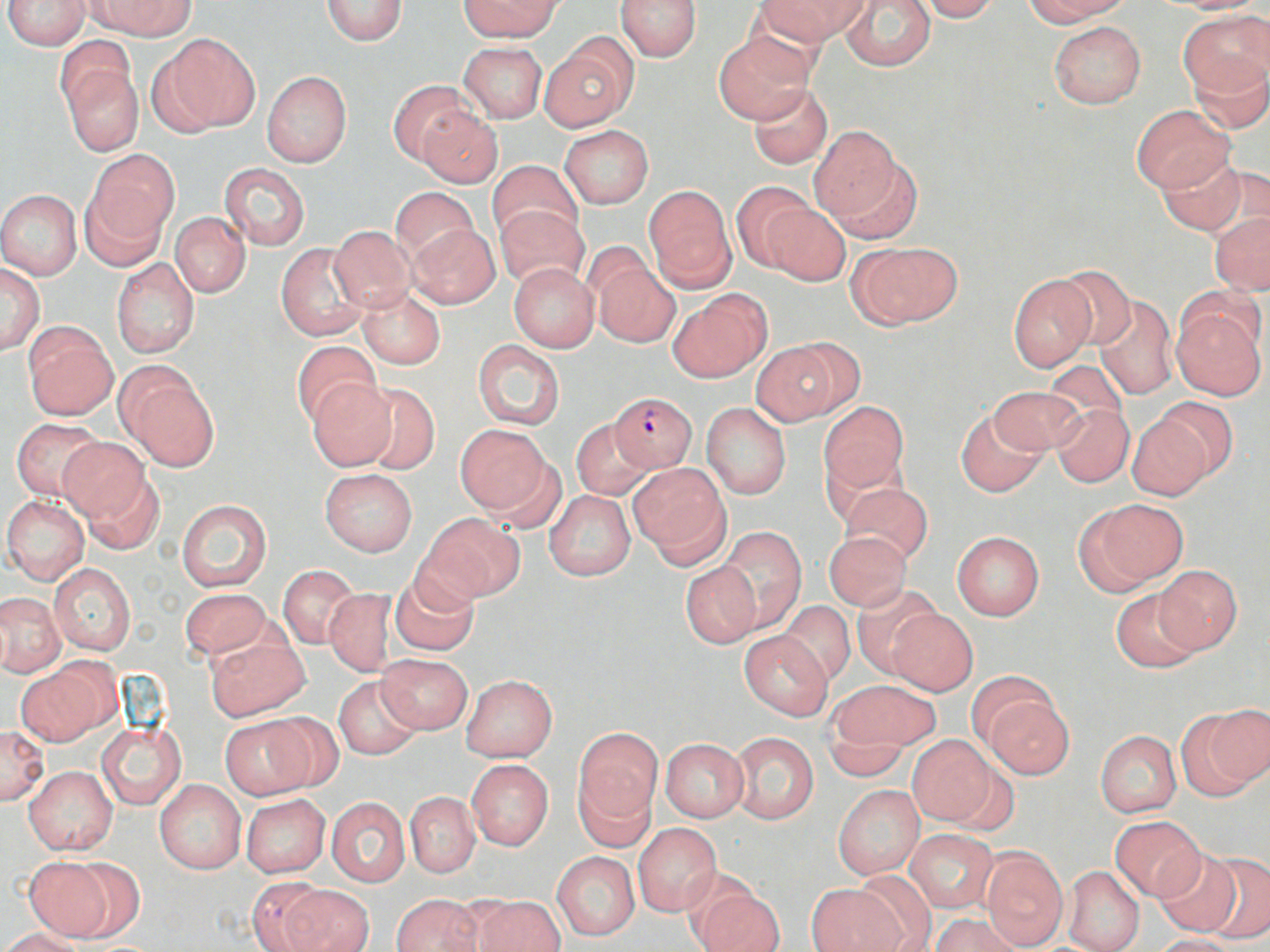

Approximate bounding boxes as [x1, y1, x2, y2] in pixels. Uninfected red blood cell locations: [4, 0, 90, 51], [91, 0, 193, 37], [321, 0, 408, 45], [461, 0, 561, 40], [615, 0, 703, 61], [758, 0, 868, 45], [915, 0, 999, 21], [1022, 0, 1129, 26], [1164, 0, 1267, 14], [839, 1, 935, 71], [1180, 10, 1268, 93], [1048, 21, 1146, 108], [160, 34, 258, 131], [714, 34, 812, 123], [541, 36, 638, 132], [459, 42, 547, 123], [58, 50, 143, 157], [1186, 56, 1270, 134], [261, 71, 352, 167], [388, 80, 469, 165], [748, 83, 833, 169], [1132, 104, 1232, 193], [417, 107, 503, 188], [808, 124, 901, 221], [560, 125, 653, 208], [85, 152, 177, 251], [829, 153, 922, 245], [1156, 153, 1250, 235], [487, 160, 582, 244], [218, 163, 310, 251], [731, 181, 813, 270], [643, 185, 735, 291], [390, 187, 480, 264], [0, 190, 82, 280], [764, 203, 851, 286], [497, 205, 588, 290], [1210, 211, 1270, 295], [171, 212, 250, 297], [408, 223, 499, 308], [328, 226, 416, 311], [851, 241, 960, 329], [275, 242, 373, 342], [111, 257, 201, 360], [592, 259, 680, 348], [508, 263, 599, 352], [0, 264, 44, 354], [1049, 264, 1140, 351], [1007, 272, 1096, 371], [355, 286, 446, 369], [669, 291, 771, 382], [1093, 295, 1178, 399], [1172, 299, 1267, 399], [23, 326, 117, 420], [291, 339, 381, 428], [751, 340, 847, 425], [472, 341, 565, 430], [116, 365, 217, 470], [307, 380, 397, 469], [354, 382, 441, 475], [986, 385, 1086, 456], [1151, 397, 1237, 485], [820, 401, 908, 493], [1051, 402, 1133, 486], [701, 404, 791, 500], [955, 408, 1048, 497], [1127, 413, 1214, 501], [11, 418, 103, 500], [571, 419, 656, 501], [454, 424, 553, 516], [58, 436, 147, 523], [631, 465, 730, 565], [79, 466, 166, 555], [320, 469, 417, 555], [839, 483, 933, 565], [545, 490, 636, 581], [2, 495, 89, 584], [175, 497, 272, 593], [1078, 497, 1189, 592], [421, 513, 523, 604], [716, 526, 806, 632], [823, 530, 911, 610], [952, 531, 1045, 620], [49, 562, 136, 655], [680, 562, 760, 648], [1154, 564, 1242, 653], [278, 565, 360, 648], [389, 570, 480, 657], [851, 582, 942, 676], [1111, 586, 1205, 673], [178, 587, 272, 662], [323, 589, 395, 676], [0, 593, 66, 675], [779, 601, 855, 685], [885, 607, 978, 695], [739, 630, 833, 720], [203, 633, 310, 722], [375, 654, 472, 734], [17, 659, 113, 744], [460, 675, 557, 762], [333, 677, 424, 760], [825, 679, 941, 757], [979, 688, 1075, 779], [1183, 704, 1270, 797], [219, 715, 318, 800], [97, 721, 185, 809], [0, 724, 48, 804], [574, 728, 661, 828], [1096, 730, 1181, 817], [731, 733, 818, 824], [907, 737, 998, 827], [660, 738, 747, 822], [466, 759, 554, 851], [24, 766, 117, 854], [575, 770, 656, 853], [156, 780, 245, 874], [833, 786, 924, 879], [405, 792, 480, 877], [242, 793, 330, 878], [326, 797, 410, 887], [1108, 815, 1205, 901], [633, 823, 721, 917], [906, 830, 996, 912], [980, 847, 1069, 949], [1151, 850, 1244, 935], [1198, 850, 1270, 943], [552, 852, 639, 939], [58, 857, 147, 938], [25, 858, 113, 939], [1063, 866, 1144, 952], [849, 869, 938, 949], [245, 875, 333, 952], [279, 884, 375, 952], [806, 885, 901, 952], [693, 887, 786, 952], [392, 894, 484, 952], [470, 894, 564, 952], [932, 913, 1023, 952], [4, 928, 87, 952], [1150, 935, 1241, 952]. Plasmodium falciparum-infected red blood cell locations: [612, 391, 696, 470]. Slide-level diagnosis: Plasmodium falciparum. Optical microscopy. Captured at 1000x magnification. Image is 1270×952 pixels. One field of a larger specimen. Thin blood film. May-Grünwald-Giemsa-stained preparation.